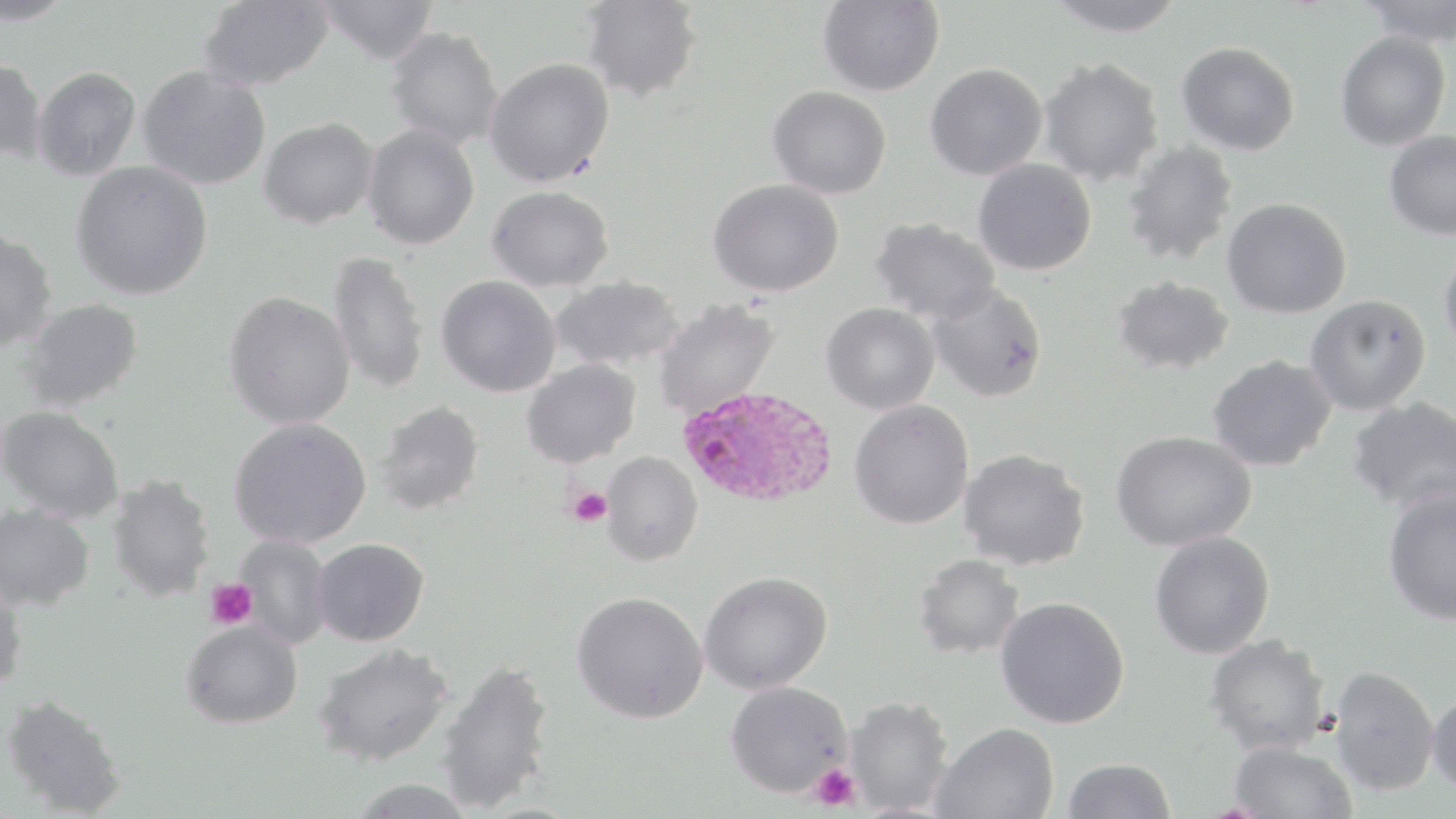
slide-level diagnosis = Plasmodium ovale
preparation = thin blood film
uninfected red blood cell locations = approximate bounding boxes as named x1/y1/x2/y2 corners in pixels: (x1=0, y1=0, x2=74, y2=26), (x1=197, y1=0, x2=335, y2=92), (x1=315, y1=0, x2=440, y2=66), (x1=818, y1=0, x2=945, y2=96), (x1=1043, y1=0, x2=1189, y2=37), (x1=1356, y1=0, x2=1456, y2=47), (x1=580, y1=1, x2=703, y2=103), (x1=385, y1=27, x2=503, y2=149), (x1=1335, y1=31, x2=1450, y2=151), (x1=1177, y1=42, x2=1300, y2=156), (x1=0, y1=57, x2=47, y2=165), (x1=486, y1=58, x2=615, y2=188), (x1=1039, y1=58, x2=1165, y2=186), (x1=924, y1=64, x2=1047, y2=180), (x1=137, y1=65, x2=272, y2=189), (x1=33, y1=66, x2=141, y2=181), (x1=768, y1=86, x2=891, y2=199), (x1=258, y1=118, x2=378, y2=229), (x1=362, y1=125, x2=479, y2=249), (x1=1384, y1=130, x2=1456, y2=241), (x1=1120, y1=140, x2=1240, y2=266), (x1=973, y1=158, x2=1097, y2=275), (x1=71, y1=162, x2=213, y2=300), (x1=708, y1=179, x2=843, y2=297), (x1=487, y1=186, x2=614, y2=291), (x1=1223, y1=198, x2=1351, y2=318), (x1=868, y1=216, x2=1001, y2=324), (x1=0, y1=228, x2=58, y2=351), (x1=1439, y1=250, x2=1456, y2=358), (x1=328, y1=252, x2=429, y2=395), (x1=436, y1=276, x2=561, y2=397), (x1=551, y1=276, x2=686, y2=372), (x1=1112, y1=277, x2=1235, y2=376), (x1=927, y1=283, x2=1048, y2=402), (x1=224, y1=291, x2=355, y2=429), (x1=1305, y1=295, x2=1431, y2=416), (x1=20, y1=298, x2=145, y2=412), (x1=653, y1=299, x2=780, y2=419), (x1=821, y1=303, x2=939, y2=414), (x1=1208, y1=355, x2=1338, y2=471), (x1=521, y1=359, x2=641, y2=468), (x1=1347, y1=397, x2=1456, y2=516), (x1=849, y1=399, x2=974, y2=529), (x1=375, y1=400, x2=485, y2=515), (x1=1, y1=405, x2=125, y2=523), (x1=229, y1=417, x2=371, y2=549), (x1=1111, y1=430, x2=1257, y2=551), (x1=959, y1=448, x2=1091, y2=571), (x1=601, y1=451, x2=702, y2=566), (x1=106, y1=475, x2=216, y2=602), (x1=1382, y1=487, x2=1456, y2=626), (x1=0, y1=503, x2=95, y2=611), (x1=1149, y1=532, x2=1276, y2=658), (x1=235, y1=534, x2=332, y2=649), (x1=313, y1=538, x2=428, y2=646), (x1=913, y1=554, x2=1025, y2=659), (x1=698, y1=571, x2=832, y2=695), (x1=0, y1=576, x2=28, y2=693), (x1=572, y1=591, x2=708, y2=723), (x1=995, y1=596, x2=1130, y2=729), (x1=181, y1=620, x2=303, y2=729), (x1=1205, y1=634, x2=1333, y2=757), (x1=312, y1=643, x2=454, y2=767), (x1=436, y1=657, x2=556, y2=813), (x1=1328, y1=665, x2=1441, y2=797), (x1=726, y1=680, x2=853, y2=798), (x1=1426, y1=689, x2=1456, y2=797), (x1=1, y1=694, x2=127, y2=817), (x1=844, y1=695, x2=954, y2=814), (x1=931, y1=722, x2=1059, y2=818), (x1=1227, y1=741, x2=1359, y2=819), (x1=1062, y1=757, x2=1177, y2=819), (x1=346, y1=778, x2=477, y2=818)
modality = optical microscopy
image size = 1456×819 pixels
Plasmodium ovale-infected red blood cell locations = approximate bounding boxes as named x1/y1/x2/y2 corners in pixels: (x1=676, y1=385, x2=839, y2=509)
platelet locations = approximate bounding boxes as named x1/y1/x2/y2 corners in pixels: (x1=565, y1=486, x2=611, y2=527), (x1=205, y1=578, x2=258, y2=630), (x1=810, y1=762, x2=861, y2=813)
magnification = 1000x
stain = May-Grünwald-Giemsa
field of view = one of a larger specimen